Classify this cell by malaria status.
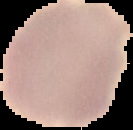
It is uninfected.

image size = 133×130 pixels
image type = cell region segmented out of the field of view; surrounding area masked to black
preparation = thin blood film